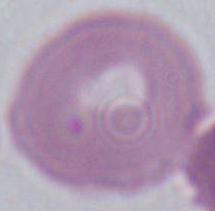
Photomicrograph. An erythrocyte is seen. Captured at 1000x magnification.